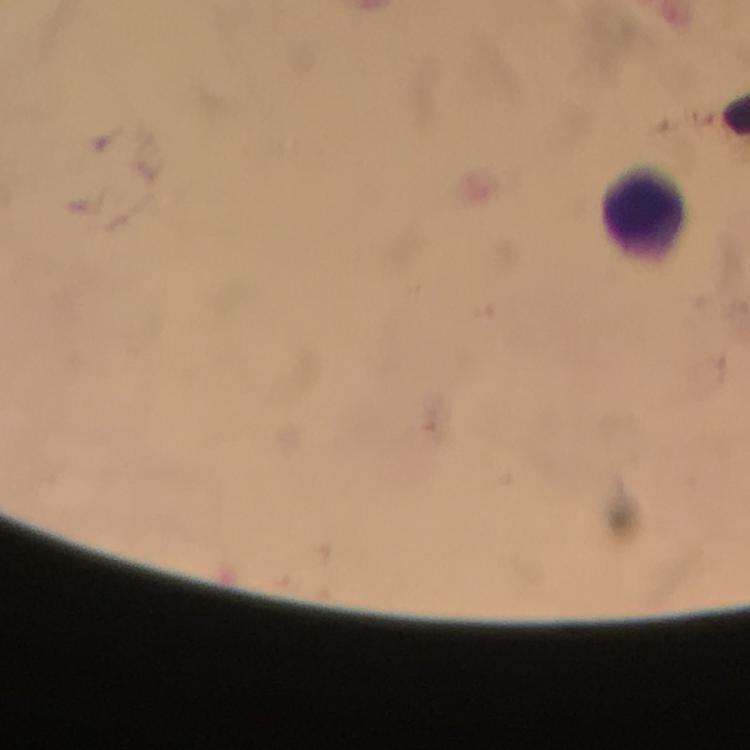
preparation: thick blood film
image_size: 750×750 pixels
immersion_oil: used
leukocyte_locations: 'approximate object centers, in pixels from the top-left corner: (x=642, y=214)'
capture: smartphone mounted on the microscope
plasmodium_parasites: none seen
cropped_from: one field of view
stain: Giemsa
magnification: 100x
context: from a diagnostic examination for malaria